Report the malaria status of this cell.
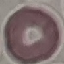
It is uninfected.

stain = Giemsa
capture = smartphone through the microscope eyepiece
image type = cell patch, automatically extracted from a larger field of view and resized to 64 × 64 pixels
preparation = thin blood smear